Report the malaria status of this cell.
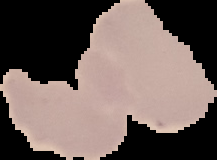
Uninfected.

Summary:
  - Preparation: thin blood film
  - Image type: cell region segmented out of the field of view; surrounding area masked to black
  - Image size: 217×160 pixels